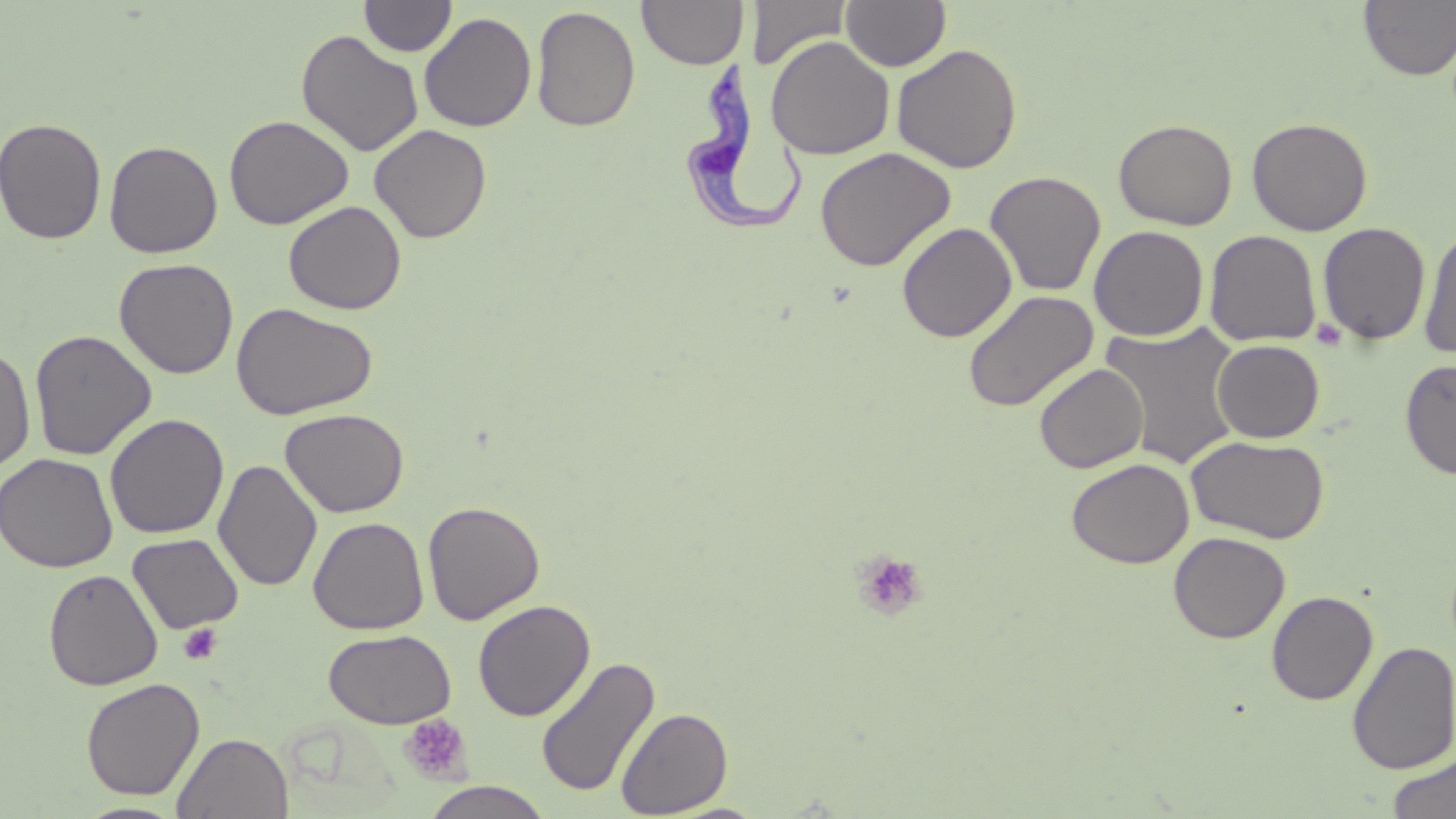 Approximate bounding boxes as (x1,y1)-(x2,y2) corner pairs in pixels. Uninfected red blood cell locations: (359,0)-(457,57), (637,0)-(749,69), (746,0)-(853,69), (841,0)-(951,71), (1358,1)-(1456,81), (531,5)-(641,132), (419,11)-(537,132), (296,30)-(424,158), (765,35)-(895,160), (892,43)-(1023,174), (224,115)-(354,229), (0,117)-(107,245), (1247,117)-(1373,236), (1114,119)-(1238,230), (369,124)-(492,243), (104,139)-(223,258), (815,146)-(957,271), (985,171)-(1106,296), (283,200)-(406,315), (896,222)-(1017,342), (1317,222)-(1431,345), (1089,225)-(1209,341), (1418,225)-(1456,359), (1205,230)-(1321,346), (114,257)-(239,379), (963,289)-(1099,412), (231,302)-(378,420), (1099,321)-(1245,469), (29,329)-(157,460), (1212,339)-(1325,443), (0,345)-(36,473), (1400,360)-(1456,481), (1034,363)-(1148,473), (280,408)-(409,518), (104,413)-(229,539), (1186,435)-(1329,544), (0,453)-(118,573), (213,458)-(322,592), (1066,458)-(1194,568), (423,500)-(545,624), (308,516)-(429,635), (1169,531)-(1290,643), (127,533)-(244,634), (43,569)-(163,690), (1267,591)-(1378,704), (472,599)-(596,721), (323,628)-(457,729), (1348,641)-(1456,774), (535,655)-(660,798), (81,677)-(204,800), (616,707)-(734,817), (172,732)-(293,818), (1387,754)-(1455,819), (420,781)-(554,819), (73,801)-(189,819). Platelet locations: (1311,317)-(1347,350), (852,550)-(929,620), (179,623)-(221,663), (399,714)-(471,784). Trypanosoma brucei locations: (690,56)-(806,240). Slide-level diagnosis: Trypanosoma brucei. May-Grünwald-Giemsa-stained preparation. Optical microscopy. Image is 1456×819 pixels. Captured at 1000x magnification. Single field of view. Thin blood film.